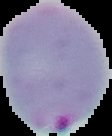
result: Plasmodium parasites identified
image_size: 112×136 pixels
image_type: segmented cell region with the area outside set to black
preparation: thin blood film